Outline each blood parasite and name the species.
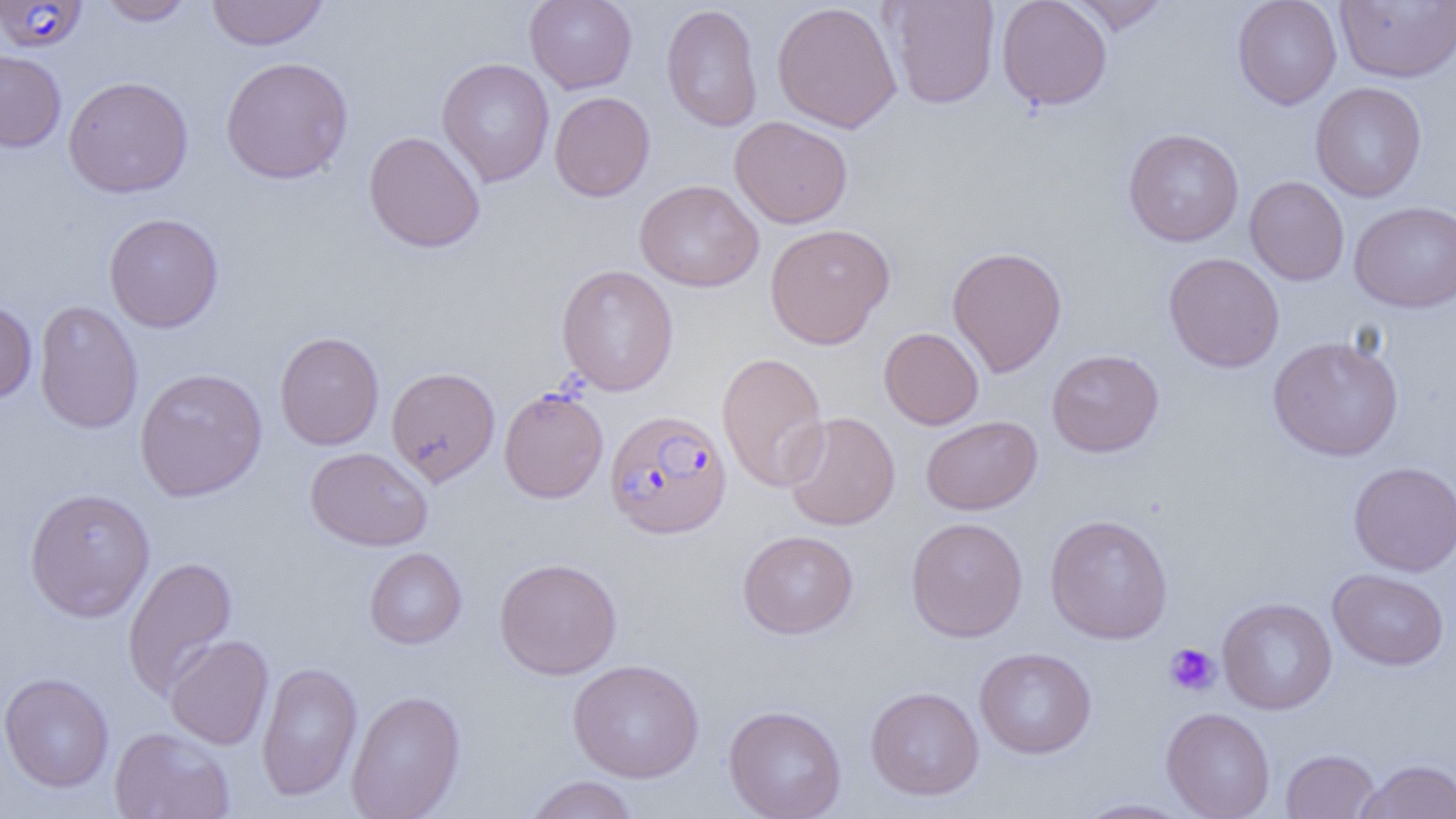

Approximate bounding boxes as (x1,y1)-(x2,y2) corner pairs in pixels.
Plasmodium falciparum-infected red blood cells: (0,1)-(88,53), (498,386)-(609,503), (604,409)-(732,539).
No Plasmodium ovale, Plasmodium malariae, Plasmodium vivax, Babesia divergens, or Trypanosoma brucei observed.

Platelet locations: (1164,643)-(1221,696). Uninfected red blood cell locations: (96,0)-(197,26), (206,0)-(329,50), (524,0)-(638,94), (885,0)-(1000,109), (996,0)-(1112,110), (1064,0)-(1171,35), (1232,0)-(1342,109), (1335,1)-(1456,83), (771,2)-(902,133), (661,3)-(763,132), (0,49)-(66,153), (220,56)-(353,184), (436,57)-(554,187), (63,76)-(194,198), (1310,81)-(1427,202), (549,91)-(655,201), (729,116)-(853,228), (1123,128)-(1244,247), (363,131)-(485,253), (1244,176)-(1349,286), (634,179)-(764,292), (1349,200)-(1455,313), (103,213)-(224,333), (765,222)-(895,348), (947,245)-(1068,377), (1163,252)-(1285,372), (556,264)-(679,396), (0,299)-(37,405), (33,300)-(143,434), (878,327)-(984,430), (274,331)-(384,450), (1267,335)-(1404,461), (1046,349)-(1164,457), (716,352)-(830,492), (134,367)-(268,501), (386,367)-(500,486), (782,411)-(900,531), (921,415)-(1042,515), (306,447)-(433,550), (1348,461)-(1456,576), (24,487)-(156,621), (1044,513)-(1174,644), (906,516)-(1028,642), (737,530)-(858,639), (364,547)-(467,649), (122,556)-(238,699), (494,557)-(622,680), (1327,569)-(1449,671), (1217,597)-(1337,715), (165,635)-(274,750), (974,647)-(1096,759), (567,658)-(704,783), (256,661)-(362,801), (0,672)-(114,793), (865,686)-(984,800), (346,690)-(466,819), (723,704)-(847,819), (1161,707)-(1275,819), (110,726)-(235,819), (1280,748)-(1381,818), (1356,758)-(1456,818), (523,775)-(639,819), (1072,797)-(1197,818). Slide-level diagnosis: Plasmodium falciparum. Image is 1456×819 pixels. Thin blood film. One field of a larger specimen. Optical microscopy. 1000x magnification.